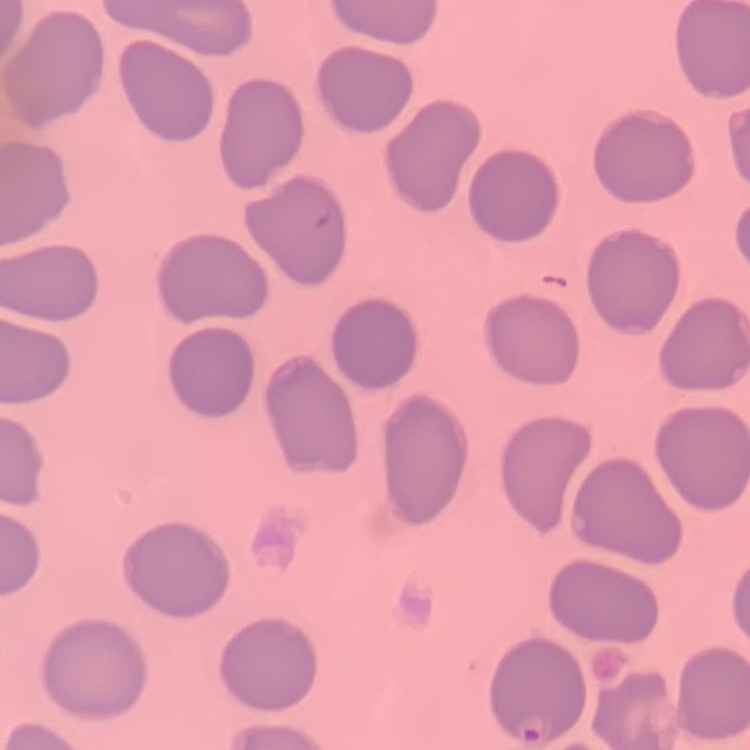

Summary:
  - Red blood cell morphology: no rouleaux formation
  - Preparation: thin blood film
  - Image type: square crop of a larger photomicrograph
  - Stain: Field's or Giemsa